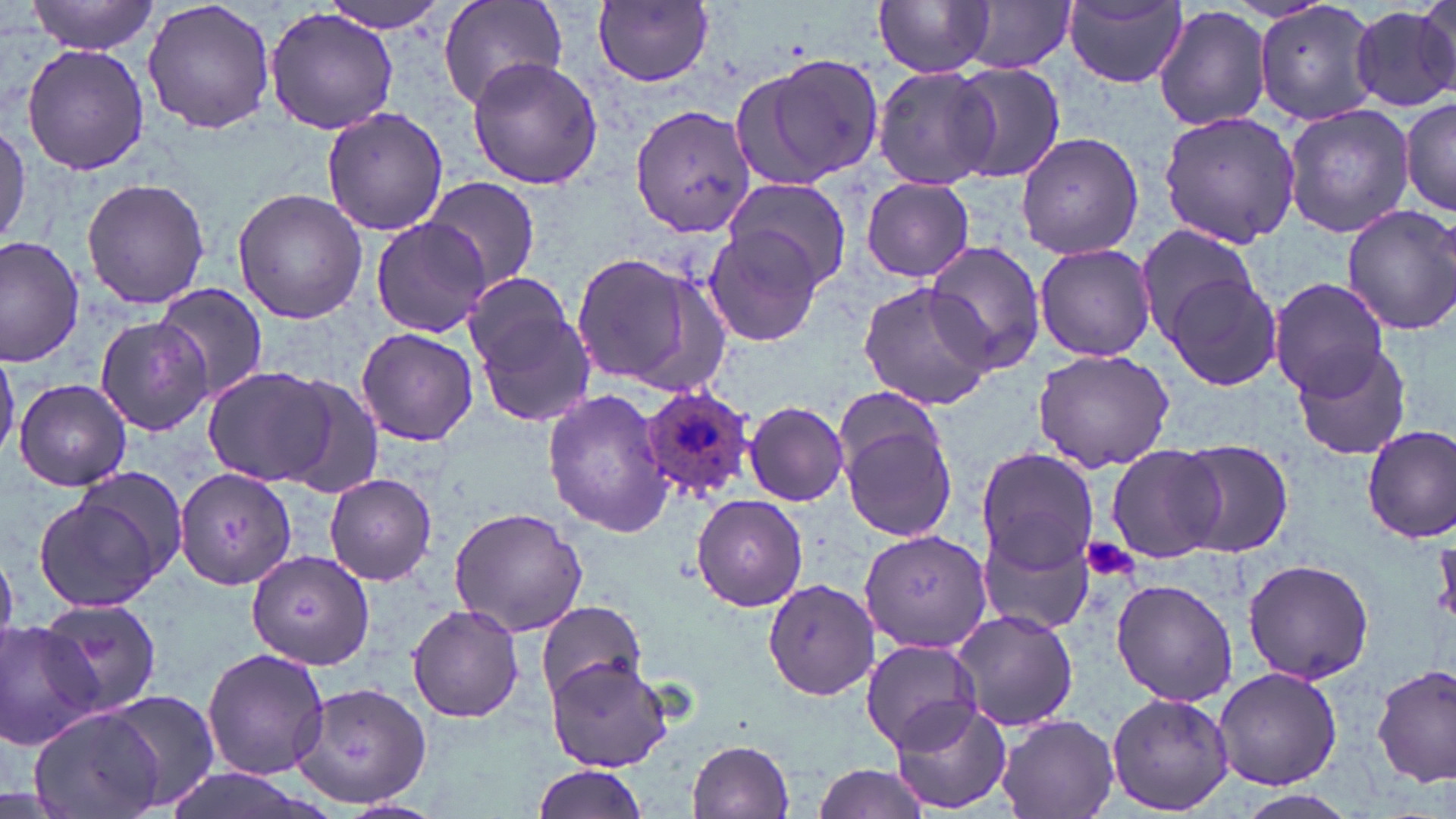
Summary:
  - Coordinate format: approximate bounding boxes as [x1, y1, x2, y2] in pixels
  - Plasmodium ovale-infected red blood cell locations: [642, 387, 756, 501]
  - Uninfected red blood cell locations: [26, 0, 158, 53], [143, 0, 275, 135], [318, 0, 457, 33], [437, 0, 567, 113], [593, 0, 716, 86], [874, 0, 992, 77], [1415, 0, 1455, 92], [1252, 1, 1382, 129], [951, 2, 1076, 75], [1059, 2, 1190, 91], [1351, 2, 1456, 113], [263, 5, 402, 136], [1154, 5, 1273, 132], [20, 43, 149, 175], [737, 52, 885, 189], [466, 56, 603, 190], [947, 62, 1065, 183], [874, 64, 997, 189], [1401, 97, 1456, 216], [631, 103, 757, 238], [1283, 104, 1415, 239], [322, 105, 448, 237], [1157, 106, 1299, 251], [1016, 132, 1144, 260], [82, 177, 210, 309], [421, 178, 542, 292], [724, 178, 856, 290], [862, 178, 975, 282], [232, 186, 370, 324], [1339, 204, 1456, 336], [369, 217, 490, 338], [1134, 222, 1263, 343], [700, 228, 827, 347], [0, 236, 82, 368], [921, 242, 1048, 374], [1034, 242, 1158, 360], [569, 250, 715, 392], [1164, 272, 1283, 391], [1271, 279, 1393, 398], [856, 281, 996, 411], [468, 284, 590, 421], [155, 285, 269, 405], [96, 316, 214, 436], [356, 326, 479, 446], [0, 342, 20, 462], [1290, 343, 1416, 462], [1030, 348, 1175, 473], [202, 365, 341, 487], [273, 374, 388, 502], [14, 378, 130, 493], [543, 389, 672, 536], [744, 401, 850, 506], [841, 415, 959, 545], [1361, 425, 1456, 543], [1176, 438, 1295, 558], [1106, 443, 1230, 564], [975, 446, 1100, 571], [174, 469, 296, 589], [324, 473, 437, 584], [34, 483, 173, 613], [692, 495, 808, 610], [448, 507, 589, 638], [978, 517, 1098, 638], [862, 529, 990, 653], [248, 551, 374, 668], [1242, 558, 1375, 685], [762, 576, 880, 700], [1110, 576, 1240, 707], [536, 599, 645, 702], [37, 603, 163, 719], [408, 604, 524, 722], [950, 608, 1078, 731], [1, 621, 104, 750], [860, 638, 981, 752], [202, 647, 330, 779], [546, 656, 674, 770], [1373, 663, 1455, 788], [1212, 666, 1342, 790], [292, 681, 431, 809], [1105, 691, 1236, 815], [107, 692, 223, 810], [889, 701, 1012, 815], [26, 706, 163, 819], [996, 714, 1119, 819], [685, 738, 795, 818], [807, 761, 938, 819], [531, 764, 654, 819], [154, 767, 334, 819], [1237, 789, 1362, 819]
  - Platelet locations: [1080, 536, 1140, 584]
  - Slide-level diagnosis: Plasmodium ovale
  - Stain: May-Grünwald-Giemsa
  - Image size: 1456×819 pixels
  - Magnification: 1000x
  - Field of view: one of a larger specimen
  - Preparation: thin blood film
  - Modality: light microscopy